Assess this cell for malaria.
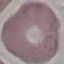

Uninfected.

preparation = thin blood film
stain = Giemsa
image type = cell patch, automatically extracted from a larger field of view and resized to 64 × 64 pixels
capture = smartphone camera at the microscope eyepiece